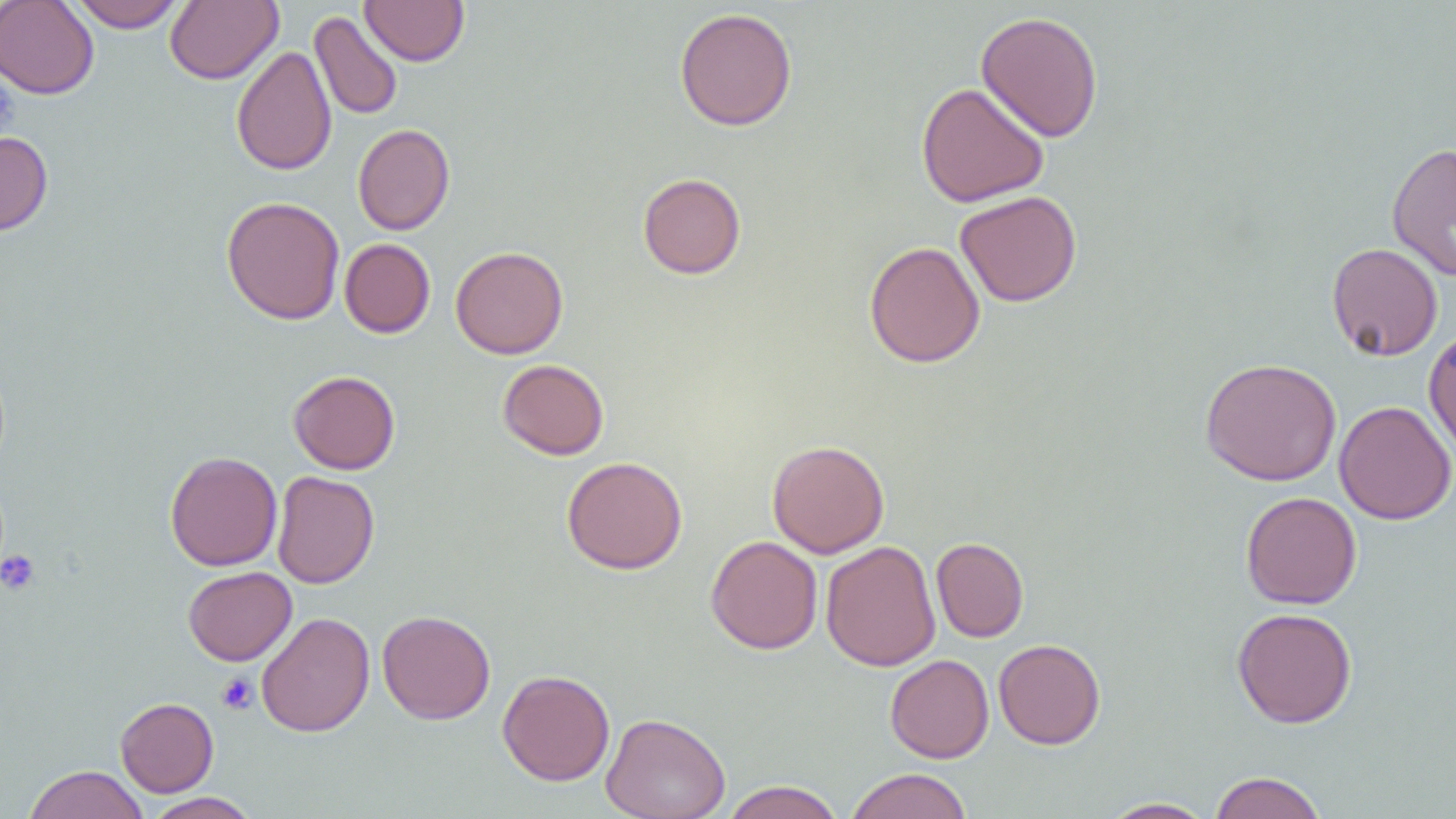
Summary:
  - Coordinate format: approximate bounding boxes as (x1, y1, x2, y2) in pixels
  - Uninfected red blood cell locations: (68, 0, 185, 32), (165, 0, 282, 85), (359, 0, 470, 66), (0, 1, 99, 99), (674, 7, 798, 131), (309, 10, 403, 121), (975, 10, 1104, 143), (231, 45, 336, 176), (916, 81, 1050, 207), (353, 123, 455, 235), (0, 131, 53, 235), (1387, 142, 1456, 282), (637, 172, 746, 279), (955, 190, 1082, 307), (221, 196, 345, 324), (339, 238, 435, 338), (863, 241, 985, 368), (1326, 242, 1443, 361), (450, 245, 569, 359), (1423, 327, 1456, 459), (1200, 357, 1341, 486), (497, 359, 609, 460), (288, 370, 400, 475), (1334, 400, 1455, 525), (766, 439, 890, 558), (165, 451, 283, 570), (561, 456, 688, 575), (272, 470, 379, 588), (1241, 491, 1362, 609), (705, 535, 823, 654), (931, 537, 1029, 642), (821, 540, 941, 671), (182, 566, 297, 666), (1231, 607, 1358, 728), (377, 609, 496, 724), (256, 612, 375, 737), (993, 638, 1105, 749), (885, 654, 994, 763), (497, 669, 615, 786), (115, 697, 219, 797), (601, 713, 731, 819), (23, 764, 148, 819), (845, 768, 973, 819), (1208, 771, 1327, 819), (721, 780, 845, 819), (144, 792, 261, 819), (1098, 797, 1215, 818)
  - Platelet locations: (0, 73, 18, 141), (0, 550, 41, 595), (216, 672, 258, 714)
  - Slide-level diagnosis: no evidence of blood parasites
  - Magnification: 1000x
  - Field of view: one of a larger specimen
  - Preparation: thin blood film
  - Modality: optical microscopy
  - Image size: 1456×819 pixels